Name the parasite shown.
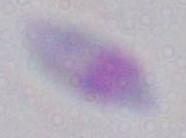

This is Toxoplasma gondii.

Captured at 1000x magnification. Photomicrograph.